State which parasite is depicted.
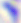
This is Toxoplasma gondii.

Summary:
  - Magnification: 400x
  - Modality: photomicrograph